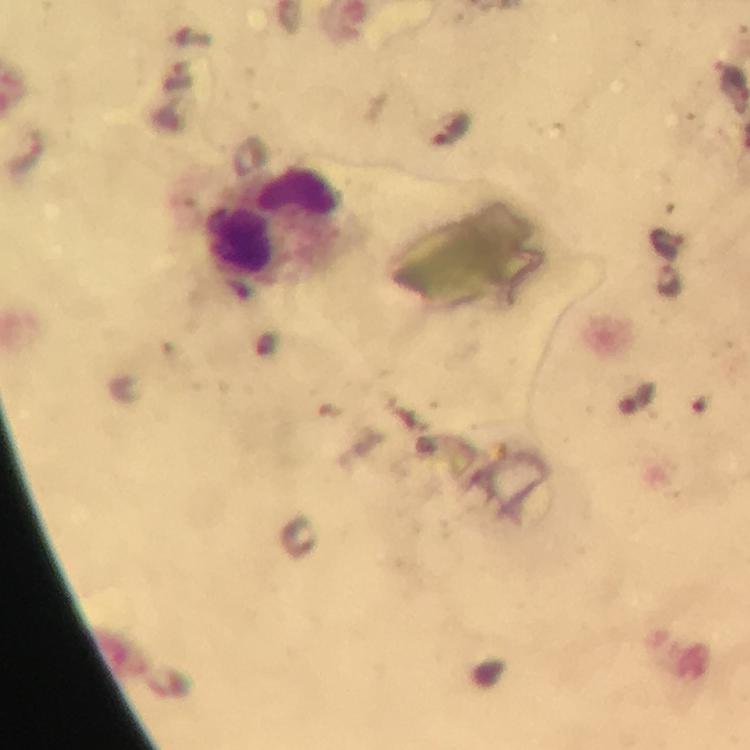
Approximate centers as {x, y} in pixels. Malaria parasite locations: {451, 129}. Leukocyte locations: {273, 227}. Immersion oil was used. 100x magnification. Giemsa-stained preparation. Photographed with a smartphone mounted on the microscope. Cropped region of a single field of view. Thick smear. From a diagnostic examination for malaria. Image is 750×750 pixels.